State the preparation type.
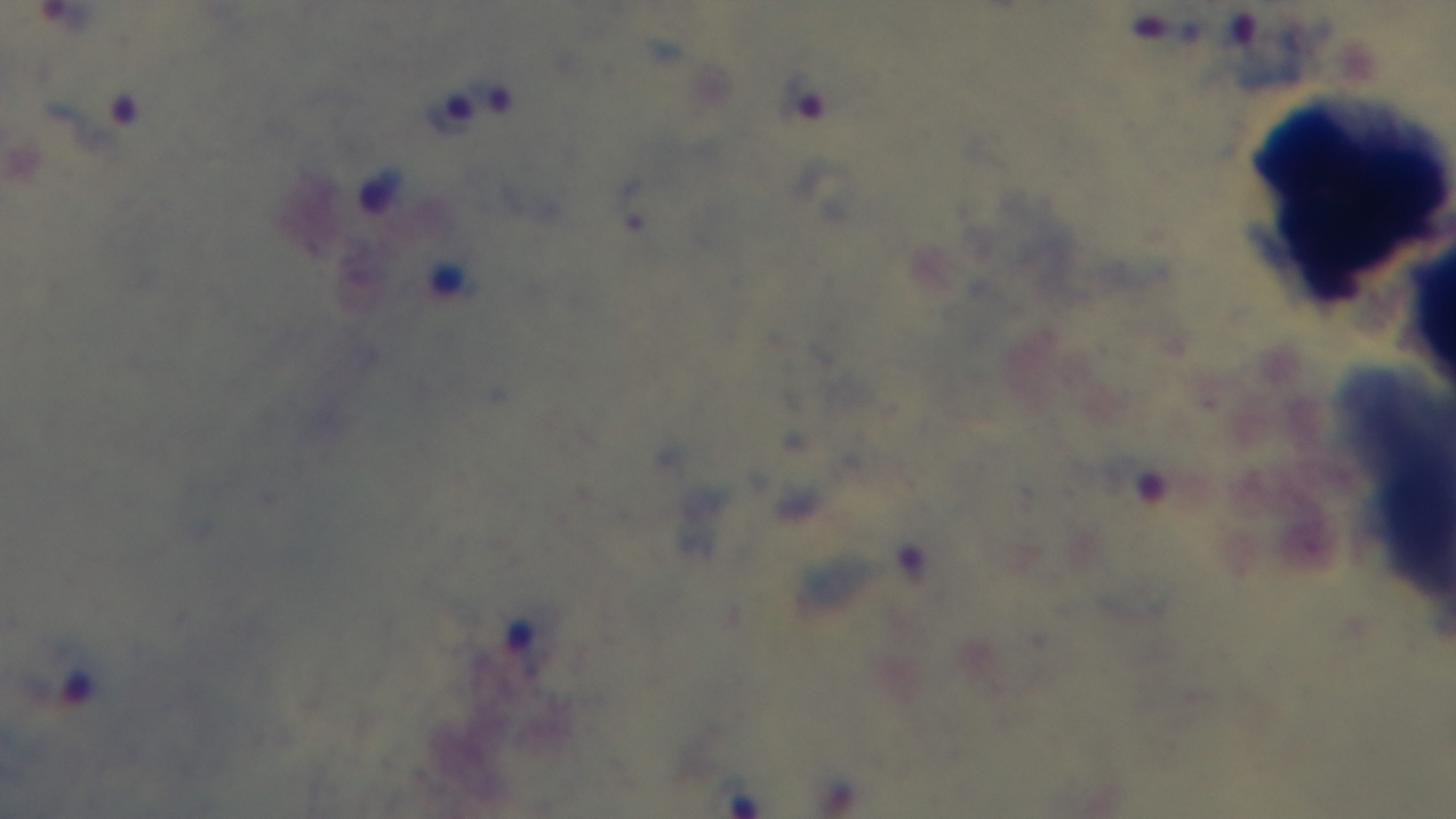
Thick.

Oil-immersion objective, 100x. Mounted 4K digital camera. Single field of view. Light microscopy. Malaria status: infected. Giemsa stain.